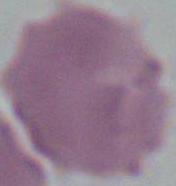
{
  "identification": "red blood cell",
  "magnification": "1000x",
  "modality": "photomicrograph"
}